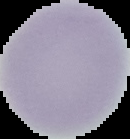
Summary:
  - Image size: 130×139 pixels
  - Image type: cell region segmented out of the field of view; surrounding area masked to black
  - Malaria status: uninfected
  - Preparation: thin blood film